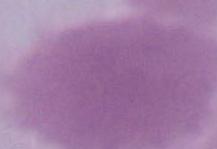
Summary:
  - Magnification: 1000x
  - Identification: red blood cell
  - Modality: micrograph